Comment on the morphology of the red blood cells.
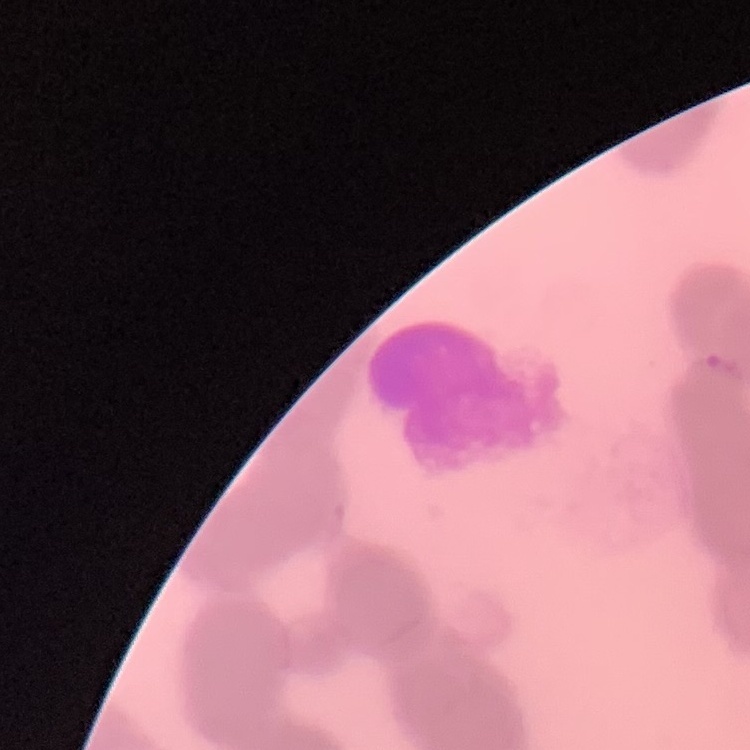
Rouleaux formation.

Thin blood film. Square crop of a larger photomicrograph. Field's or Giemsa stain.